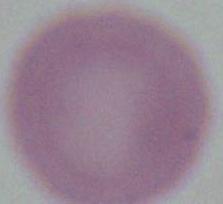 Photomicrograph. An erythrocyte is seen. 1000x magnification.